State the blood parasite species.
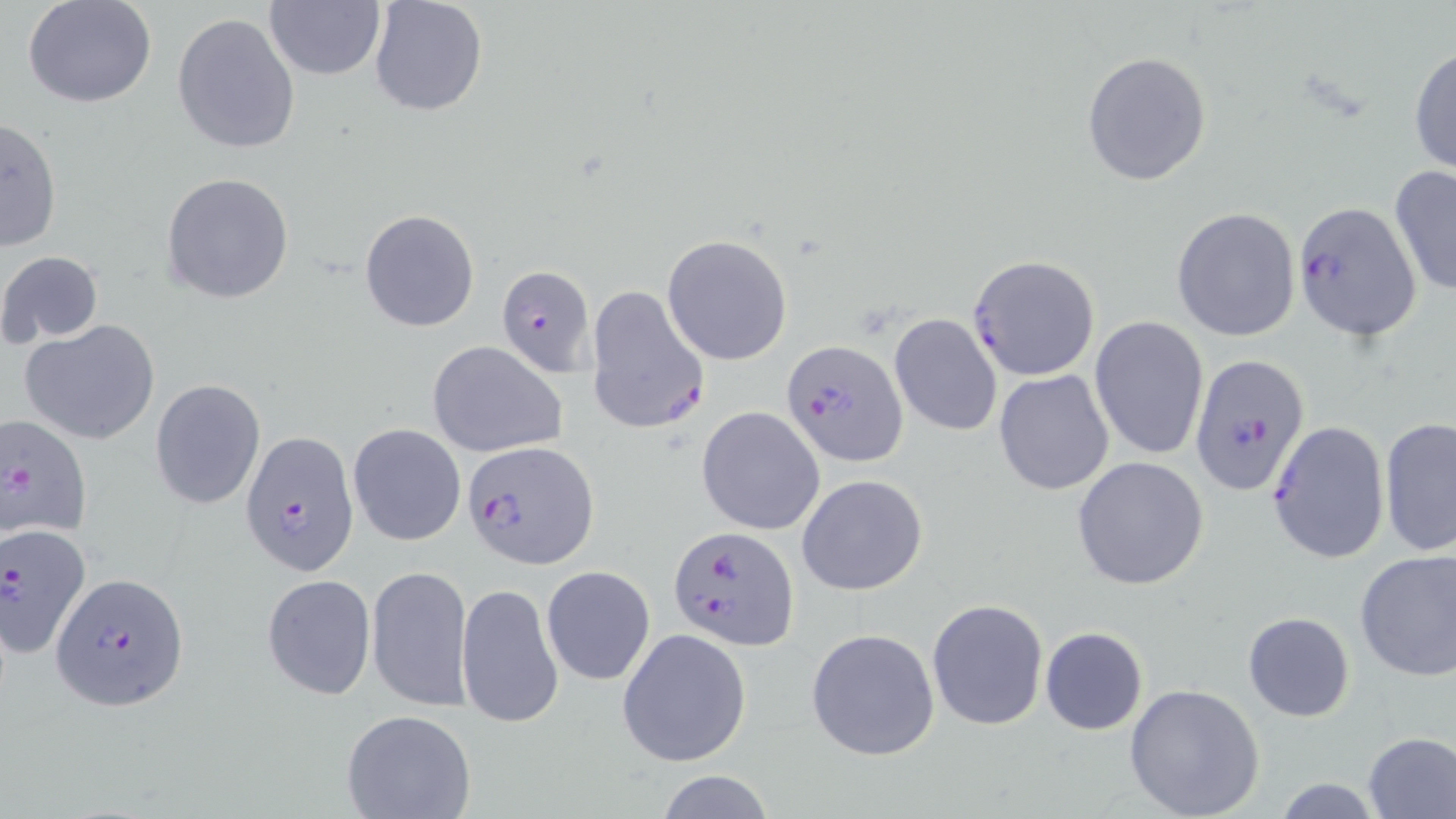

Plasmodium falciparum.

Approximate bounding boxes as (x1,y1)-(x2,y2) corner pairs in pixels. Uninfected red blood cell locations: (369,0)-(488,119), (24,1)-(158,108), (264,1)-(386,83), (172,12)-(300,154), (1408,43)-(1456,181), (1082,52)-(1212,185), (1,116)-(64,252), (1388,163)-(1456,299), (160,172)-(295,304), (359,207)-(482,333), (1171,207)-(1300,342), (662,234)-(793,364), (1,251)-(106,346), (888,313)-(1002,437), (1089,316)-(1209,462), (20,318)-(160,445), (427,341)-(568,457), (993,369)-(1115,496), (150,380)-(266,508), (696,405)-(825,535), (1378,417)-(1456,558), (1267,420)-(1389,563), (348,422)-(466,546), (1071,456)-(1210,590), (797,474)-(929,595), (1354,548)-(1456,680), (366,565)-(475,712), (541,566)-(655,685), (263,575)-(376,700), (457,580)-(564,731), (926,598)-(1049,731), (1243,612)-(1355,721), (616,626)-(752,768), (1039,626)-(1148,735), (806,627)-(940,761), (1123,682)-(1266,819), (341,708)-(476,819), (1361,732)-(1456,818), (657,771)-(774,818), (1270,778)-(1386,816). Plasmodium falciparum-infected red blood cell locations: (1290,196)-(1423,344), (967,255)-(1100,381), (494,265)-(600,378), (585,284)-(711,438), (783,340)-(908,466), (1189,353)-(1309,498), (2,413)-(93,540), (240,431)-(360,578), (462,439)-(597,572), (1,524)-(94,658), (669,525)-(799,651), (50,573)-(188,711). Light microscopy. May-Grünwald-Giemsa stain. One field of a larger specimen. 1000x magnification. Thin blood smear. Image is 1456×819 pixels.